Report the malaria status of this cell.
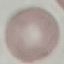
It is uninfected.

Thin blood film. Giemsa-stained preparation. Acquired by smartphone through the microscope eyepiece. Automatically extracted cell patch, resized to 64 × 64 pixels.